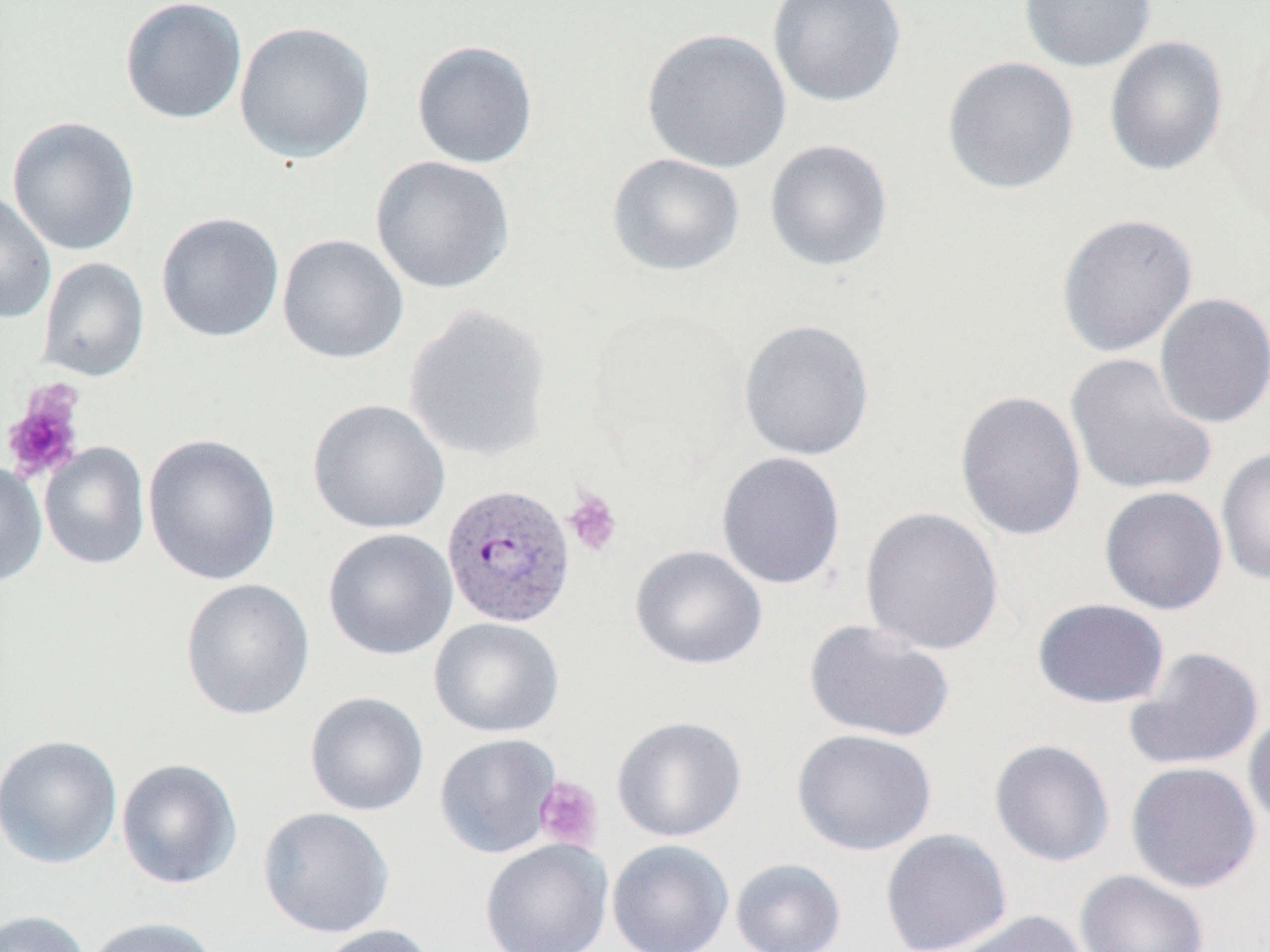

slide-level diagnosis = Plasmodium vivax
field of view = one of a larger specimen
uninfected red blood cell locations = approximate bounding boxes as (x1, y1, x2, y2) in pixels: (767, 0, 906, 108), (1017, 0, 1158, 72), (119, 1, 248, 124), (234, 20, 375, 163), (641, 27, 792, 173), (1104, 35, 1229, 177), (411, 39, 539, 169), (942, 55, 1080, 195), (6, 115, 141, 256), (764, 139, 893, 272), (606, 152, 745, 277), (370, 156, 515, 295), (0, 189, 57, 325), (156, 212, 285, 343), (1055, 212, 1198, 358), (277, 233, 409, 364), (36, 257, 150, 382), (1154, 293, 1270, 428), (404, 305, 553, 463), (738, 318, 875, 461), (1065, 353, 1217, 497), (954, 390, 1086, 541), (307, 398, 451, 535), (142, 433, 282, 587), (39, 442, 150, 570), (1216, 447, 1270, 585), (716, 451, 847, 590), (0, 460, 47, 588), (1099, 486, 1227, 615), (859, 506, 1004, 656), (322, 528, 458, 661), (630, 545, 768, 670), (180, 578, 315, 721), (1032, 598, 1170, 709), (429, 617, 565, 738), (803, 619, 956, 744), (1124, 646, 1264, 771), (304, 691, 429, 816), (1243, 707, 1270, 833), (611, 715, 747, 842), (791, 728, 937, 856), (0, 733, 122, 869), (434, 733, 561, 858), (989, 739, 1115, 867), (116, 758, 242, 889), (1125, 761, 1261, 893), (257, 806, 395, 938), (880, 828, 1013, 952), (480, 838, 613, 952), (607, 839, 734, 952), (730, 857, 846, 952), (1075, 869, 1209, 952), (0, 909, 94, 952), (948, 910, 1089, 952), (83, 916, 220, 952), (313, 924, 438, 952)
image size = 1270×952 pixels
platelet locations = approximate bounding boxes as (x1, y1, x2, y2) in pixels: (1, 380, 87, 484), (562, 487, 623, 558), (534, 776, 603, 851)
preparation = thin blood film
magnification = 1000x
modality = optical microscopy
stain = May-Grünwald-Giemsa
Plasmodium vivax-infected red blood cell locations = approximate bounding boxes as (x1, y1, x2, y2) in pixels: (440, 482, 576, 629)